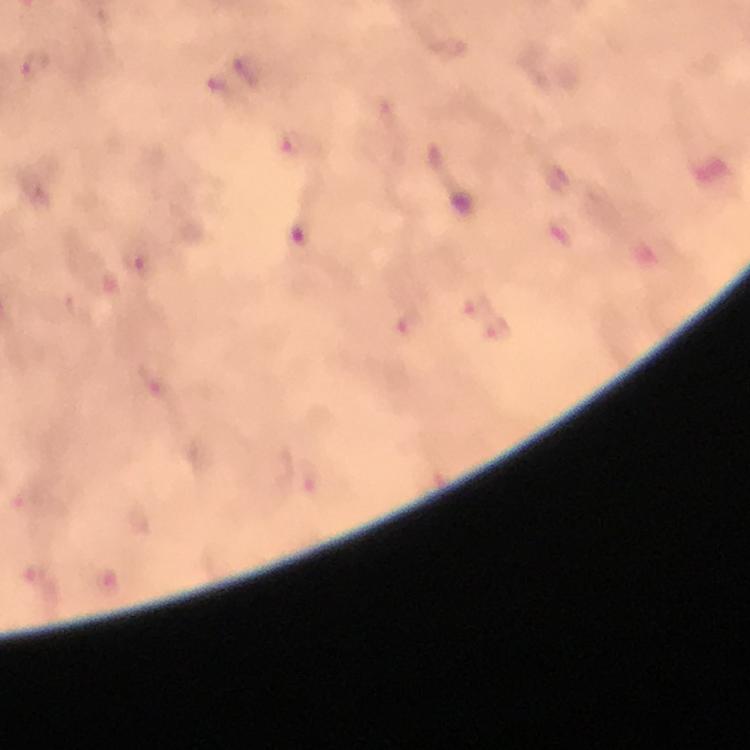
Approximate centers as {x, y} in pixels.
Summary:
  - Plasmodium parasite locations: {301, 236}
  - Capture: smartphone mounted on the microscope
  - Context: from a diagnostic examination for malaria
  - Magnification: 100x
  - Immersion oil: used
  - Cropped from: a single field of view
  - Stain: Giemsa
  - Preparation: thick blood smear
  - Image size: 750×750 pixels